Describe the morphology of the red blood cells.
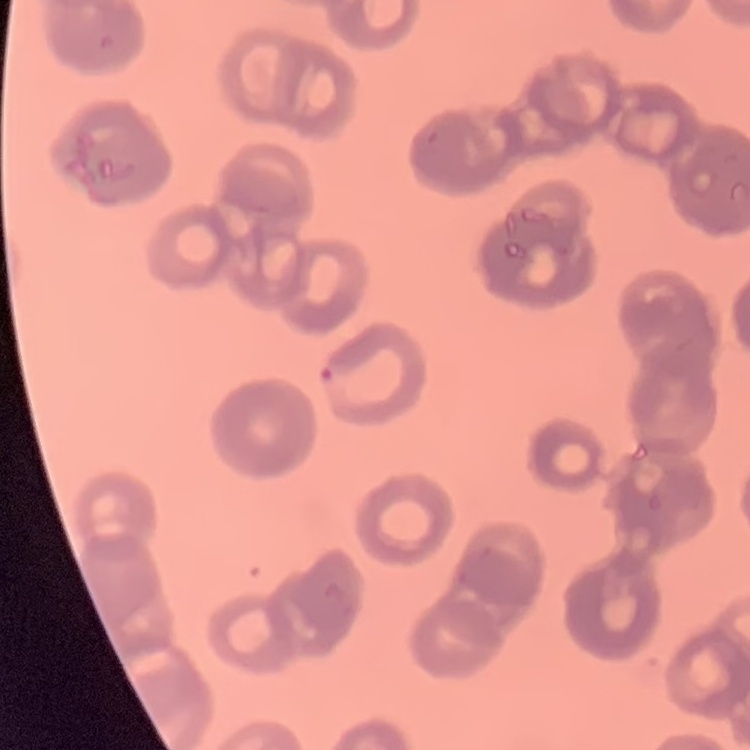
Rouleaux formation.

Thin blood film. Square crop of a larger photomicrograph. Field's or Giemsa stain.